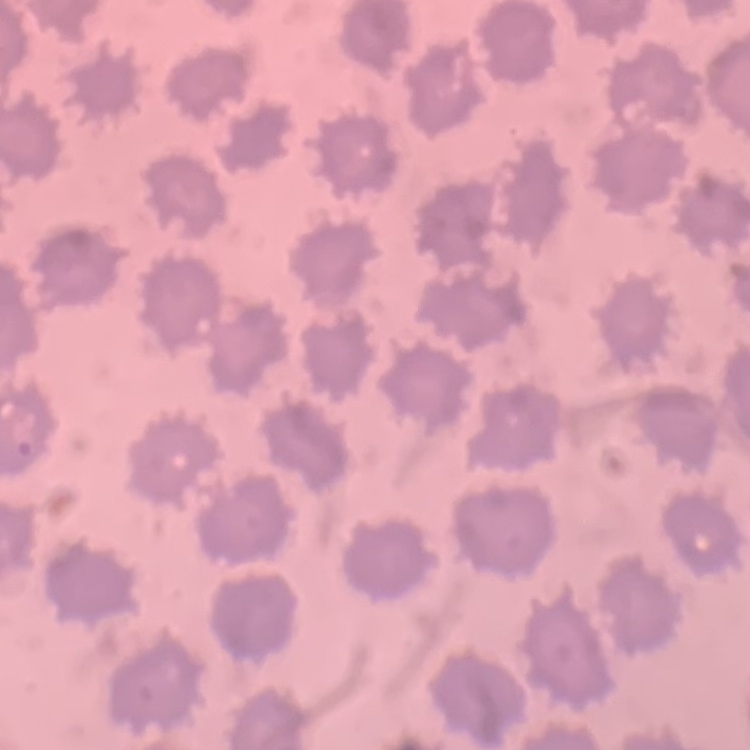
{
  "red_blood_cell_morphology": "no rouleaux formation",
  "stain": "Field's or Giemsa",
  "preparation": "thin blood film",
  "image_type": "square crop of a larger photomicrograph"
}